Name the cell type shown.
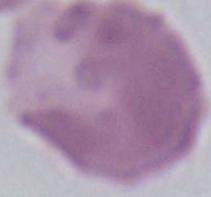

An erythrocyte.

Summary:
  - Modality: micrograph
  - Magnification: 1000x